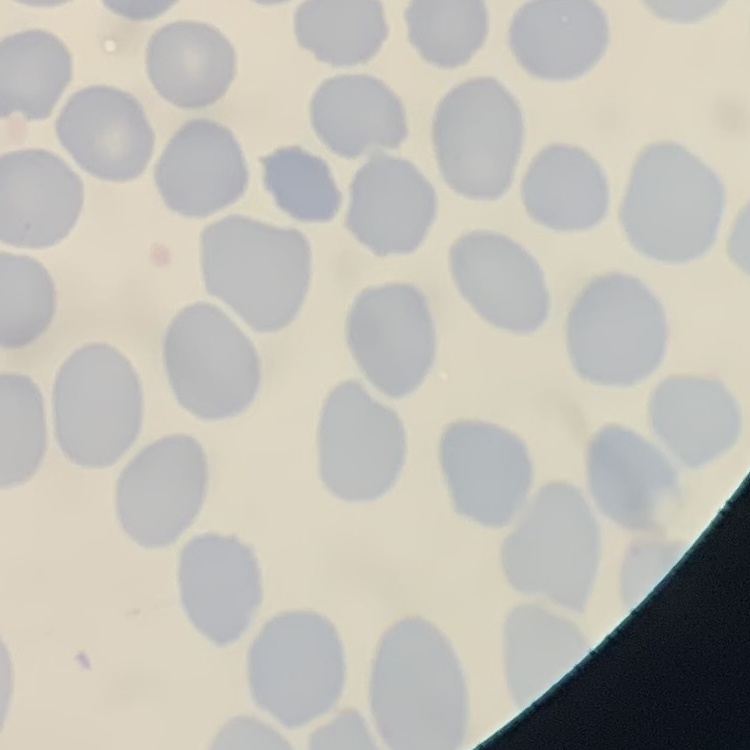
erythrocyte morphology = no rouleaux formation
preparation = thin blood smear
image type = square crop of a larger photomicrograph
stain = Field's or Giemsa